Assess this cell for malaria.
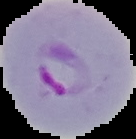
It is parasitized.

Summary:
  - Image size: 136×139 pixels
  - Image type: segmented cell region on a black background
  - Preparation: thin blood smear